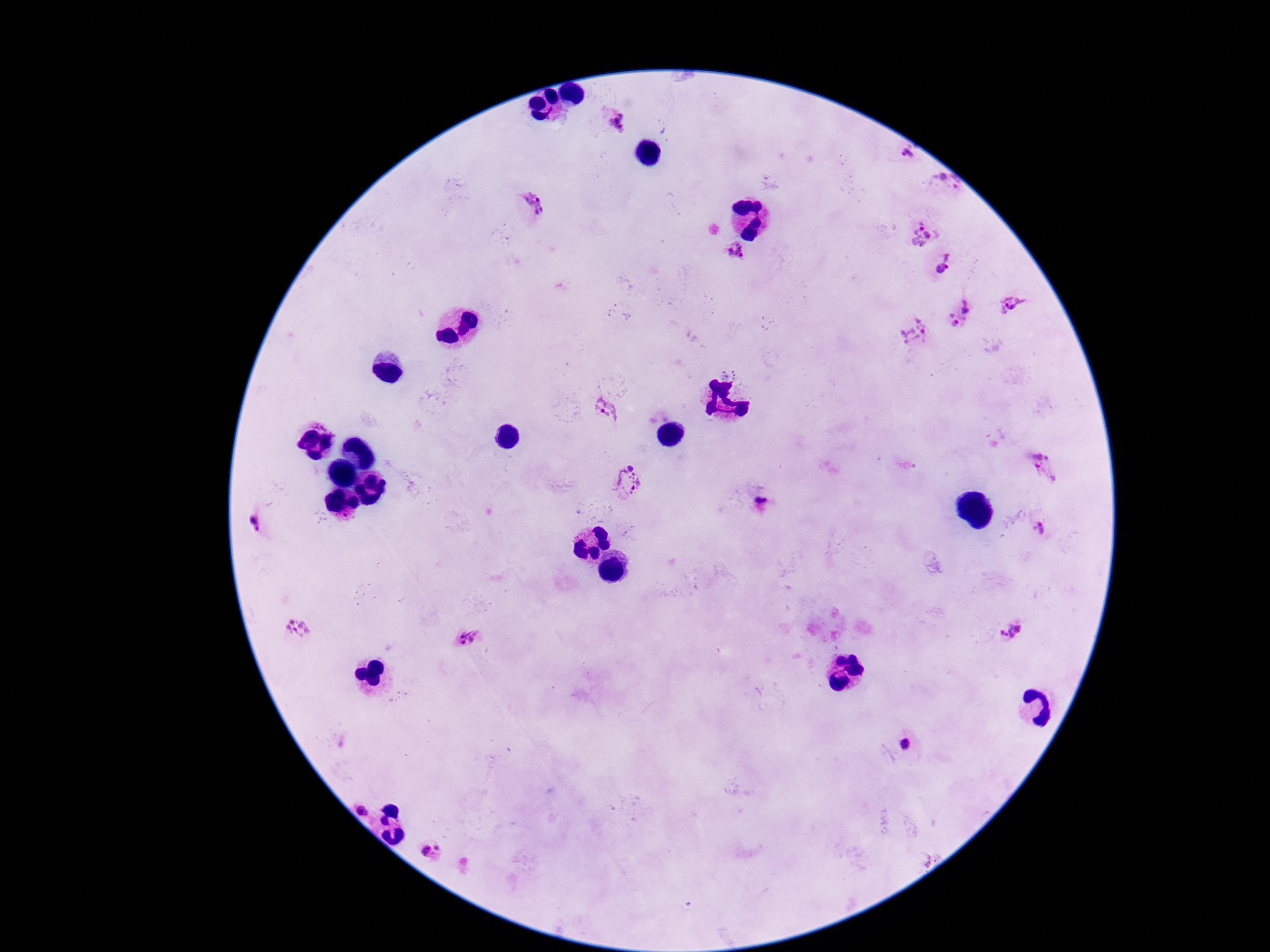
Approximate centers as (x, y) in pixels.
Summary:
  - Plasmodium parasite locations: (616, 120), (910, 154), (944, 186), (530, 208), (921, 233), (735, 252), (949, 257), (941, 269), (1012, 305), (960, 314), (914, 333), (605, 411), (322, 419), (1046, 467), (628, 481), (762, 498), (259, 521), (1040, 530), (298, 629), (1012, 631), (468, 639), (905, 744), (363, 808), (435, 853)
  - Field of view: one from this slide
  - Image size: 1270×952 pixels
  - Preparation: thick blood smear
  - Stain: Giemsa
  - Patient malaria status: positive
  - Capture: smartphone camera through the microscope eyepiece
  - Magnification: 100x